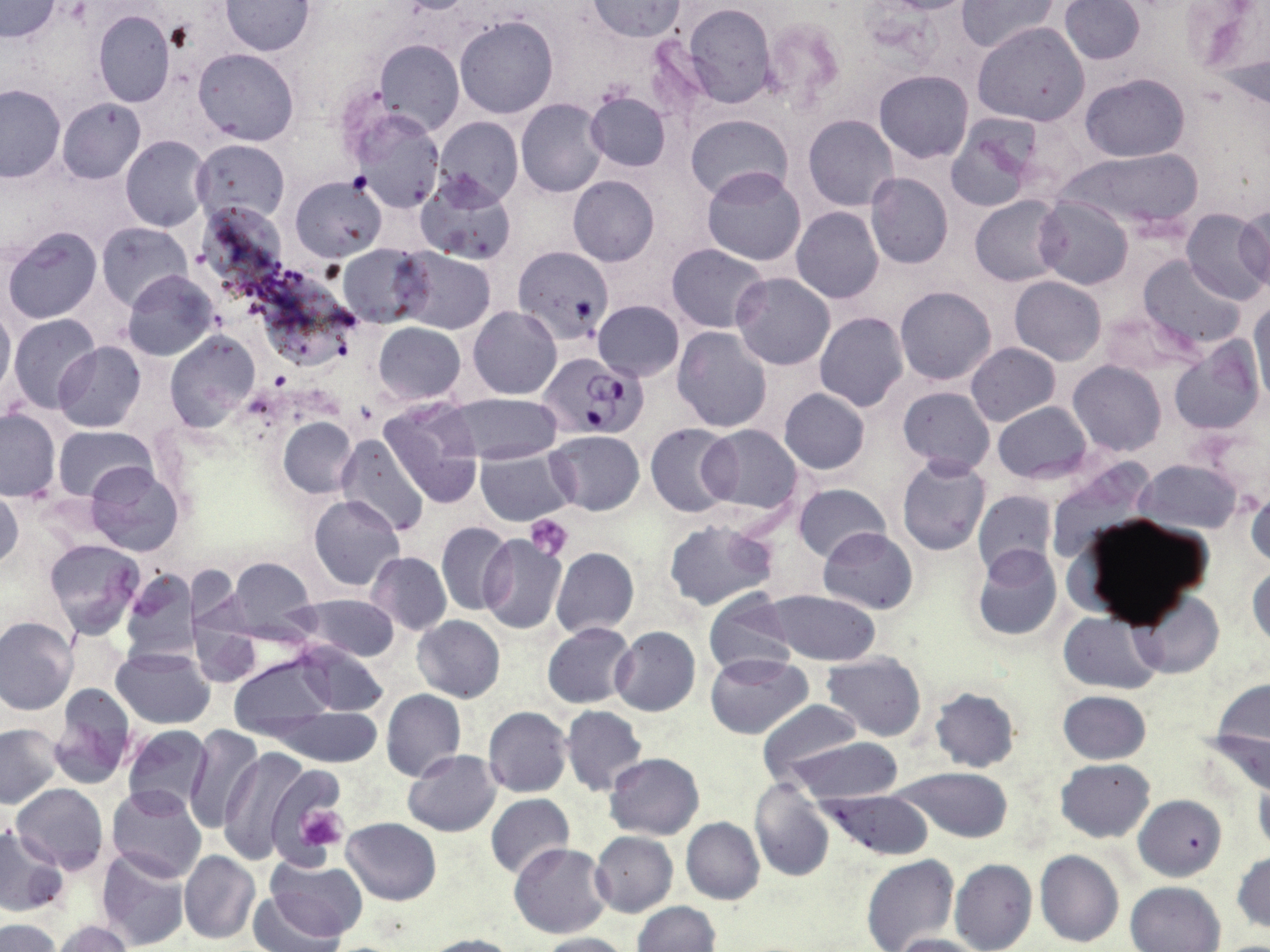

Approximate bounding boxes as (x1,y1)-(x2,y2) corner pairs in pixels. Platelet locations: (527,512)-(576,561), (296,805)-(349,852). Uninfected red blood cell locations: (220,0)-(316,55), (588,0)-(687,41), (875,0)-(979,14), (958,0)-(1058,52), (0,1)-(60,42), (1058,1)-(1145,65), (1186,1)-(1269,97), (682,3)-(777,108), (92,10)-(175,107), (454,14)-(559,119), (761,16)-(846,113), (973,22)-(1090,126), (374,39)-(465,135), (194,48)-(299,145), (874,70)-(972,162), (1080,72)-(1189,163), (0,83)-(65,181), (586,91)-(671,172), (58,98)-(145,183), (517,99)-(608,197), (351,108)-(445,213), (685,114)-(792,202), (803,114)-(898,212), (434,116)-(524,208), (945,116)-(1045,211), (120,135)-(211,231), (192,140)-(289,227), (1057,151)-(1205,233), (701,167)-(807,267), (865,172)-(953,269), (415,174)-(516,266), (569,175)-(660,266), (290,176)-(386,262), (970,196)-(1065,286), (1035,197)-(1133,289), (792,206)-(883,303), (1235,207)-(1270,289), (1182,209)-(1270,304), (96,222)-(193,309), (2,226)-(102,325), (338,243)-(432,328), (666,243)-(770,332), (396,249)-(495,334), (1138,255)-(1248,354), (121,269)-(220,361), (731,272)-(835,370), (1009,276)-(1107,366), (895,286)-(997,386), (593,299)-(684,380), (0,303)-(14,397), (1250,303)-(1270,407), (468,307)-(561,400), (815,312)-(908,412), (8,313)-(101,416), (374,323)-(465,403), (673,326)-(772,431), (166,331)-(260,433), (1169,340)-(1261,435), (53,342)-(145,432), (966,342)-(1061,427), (1068,361)-(1167,456), (898,385)-(995,478), (779,388)-(869,474), (450,393)-(562,464), (379,397)-(486,509), (993,403)-(1091,484), (0,408)-(60,501), (279,417)-(357,498), (645,424)-(737,517), (700,424)-(804,515), (53,425)-(155,503), (546,430)-(645,515), (337,434)-(429,537), (474,450)-(576,525), (896,456)-(990,556), (1138,459)-(1244,534), (86,462)-(185,557), (1045,462)-(1154,561), (793,483)-(890,562), (0,488)-(23,573), (1245,489)-(1270,569), (973,490)-(1057,579), (309,496)-(404,591), (662,520)-(780,612), (436,521)-(513,617), (819,527)-(918,613), (477,533)-(566,635), (43,539)-(144,638), (972,544)-(1061,641), (551,547)-(638,637), (367,551)-(451,635), (229,557)-(316,640), (1247,561)-(1270,651), (183,564)-(239,627), (121,568)-(200,665), (703,589)-(797,678), (765,590)-(882,666), (1129,590)-(1224,678), (295,594)-(399,661), (1058,610)-(1163,695), (190,615)-(262,689), (412,615)-(505,702), (0,616)-(78,715), (542,623)-(635,708), (610,627)-(701,715), (293,642)-(388,718), (112,648)-(215,729), (705,652)-(812,739), (821,653)-(927,741), (228,656)-(333,740), (1205,679)-(1270,797), (48,686)-(138,790), (930,686)-(1020,772), (381,689)-(466,780), (1057,690)-(1151,763), (757,700)-(864,786), (562,705)-(647,795), (483,706)-(571,797), (277,708)-(381,766), (0,722)-(63,808), (123,724)-(213,816), (183,724)-(262,832), (788,738)-(905,803), (218,746)-(307,862), (403,750)-(502,836), (604,753)-(705,839), (1055,759)-(1155,842), (894,767)-(1014,842), (748,778)-(834,881), (1253,779)-(1270,855), (13,784)-(108,872), (105,786)-(206,883), (817,790)-(935,859), (485,794)-(575,879), (1134,795)-(1227,881), (342,817)-(442,905), (681,817)-(765,905), (0,826)-(68,916), (590,832)-(677,916), (510,843)-(613,939), (96,849)-(193,951), (179,850)-(259,945), (1035,850)-(1123,948), (1231,852)-(1270,936), (861,854)-(959,952), (949,858)-(1036,952), (263,859)-(367,941), (1125,881)-(1225,952), (248,892)-(347,952), (632,901)-(719,951), (3,920)-(61,952), (50,920)-(135,952), (530,932)-(632,951), (417,933)-(521,952), (888,933)-(985,952). Plasmodium falciparum-infected red blood cell locations: (513,246)-(613,342), (540,354)-(645,439). Slide-level diagnosis: Plasmodium falciparum. May-Grünwald-Giemsa-stained preparation. Image is 1270×952 pixels. Thin blood smear. Optical microscopy. One field of a larger specimen. Captured at 1000x magnification.